Outline each blood parasite and name the species.
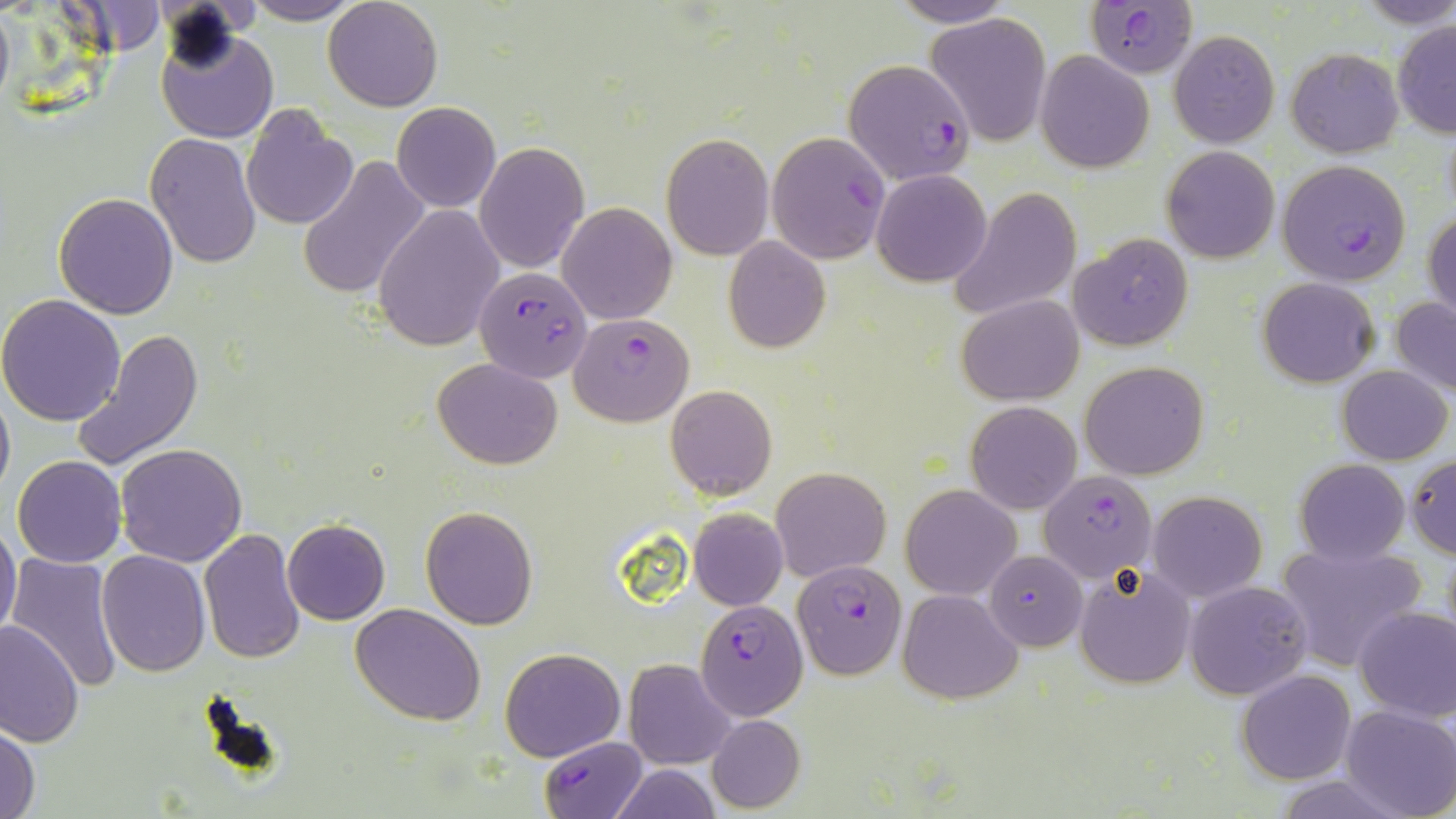

Approximate bounding boxes as named x1/y1/x2/y2 corners in pixels.
Plasmodium falciparum-infected red blood cells: (x1=1086, y1=1, x2=1198, y2=78), (x1=844, y1=60, x2=977, y2=187), (x1=1275, y1=159, x2=1412, y2=285), (x1=475, y1=264, x2=592, y2=382), (x1=569, y1=314, x2=692, y2=425), (x1=1040, y1=470, x2=1155, y2=584), (x1=984, y1=549, x2=1087, y2=650), (x1=793, y1=559, x2=905, y2=679), (x1=697, y1=600, x2=807, y2=719), (x1=538, y1=737, x2=650, y2=819).
No Plasmodium ovale, Plasmodium malariae, Plasmodium vivax, Babesia divergens, or Trypanosoma brucei observed.

Uninfected red blood cell locations: (x1=242, y1=0, x2=364, y2=24), (x1=322, y1=0, x2=444, y2=112), (x1=889, y1=0, x2=1014, y2=28), (x1=0, y1=4, x2=14, y2=115), (x1=926, y1=13, x2=1053, y2=145), (x1=1393, y1=20, x2=1456, y2=137), (x1=157, y1=26, x2=278, y2=144), (x1=1168, y1=30, x2=1279, y2=146), (x1=1285, y1=48, x2=1404, y2=158), (x1=1035, y1=50, x2=1154, y2=172), (x1=391, y1=102, x2=501, y2=212), (x1=240, y1=108, x2=358, y2=228), (x1=145, y1=132, x2=263, y2=268), (x1=765, y1=132, x2=889, y2=264), (x1=662, y1=133, x2=773, y2=260), (x1=476, y1=143, x2=588, y2=272), (x1=1162, y1=145, x2=1279, y2=263), (x1=297, y1=152, x2=430, y2=298), (x1=872, y1=169, x2=991, y2=286), (x1=947, y1=187, x2=1081, y2=320), (x1=54, y1=193, x2=179, y2=318), (x1=557, y1=202, x2=679, y2=323), (x1=373, y1=204, x2=504, y2=352), (x1=1425, y1=209, x2=1456, y2=323), (x1=1068, y1=232, x2=1193, y2=350), (x1=724, y1=236, x2=830, y2=352), (x1=1257, y1=278, x2=1380, y2=386), (x1=957, y1=294, x2=1084, y2=405), (x1=1390, y1=294, x2=1456, y2=398), (x1=0, y1=296, x2=127, y2=425), (x1=72, y1=328, x2=203, y2=470), (x1=433, y1=356, x2=562, y2=469), (x1=1081, y1=361, x2=1208, y2=479), (x1=1335, y1=365, x2=1452, y2=464), (x1=0, y1=381, x2=15, y2=505), (x1=665, y1=385, x2=776, y2=499), (x1=966, y1=401, x2=1081, y2=516), (x1=115, y1=443, x2=248, y2=567), (x1=1406, y1=453, x2=1456, y2=557), (x1=11, y1=456, x2=126, y2=568), (x1=1295, y1=458, x2=1410, y2=566), (x1=771, y1=467, x2=890, y2=582), (x1=901, y1=485, x2=1020, y2=599), (x1=1149, y1=490, x2=1267, y2=601), (x1=421, y1=507, x2=537, y2=628), (x1=689, y1=509, x2=788, y2=610), (x1=281, y1=518, x2=389, y2=625), (x1=0, y1=519, x2=22, y2=642), (x1=198, y1=528, x2=305, y2=666), (x1=1273, y1=540, x2=1427, y2=673), (x1=95, y1=551, x2=210, y2=677), (x1=7, y1=552, x2=123, y2=691), (x1=1074, y1=563, x2=1197, y2=689), (x1=1185, y1=580, x2=1312, y2=700), (x1=898, y1=589, x2=1020, y2=703), (x1=350, y1=603, x2=486, y2=726), (x1=1355, y1=606, x2=1456, y2=723), (x1=0, y1=621, x2=84, y2=749), (x1=500, y1=647, x2=625, y2=761), (x1=623, y1=659, x2=735, y2=769), (x1=1238, y1=669, x2=1356, y2=784), (x1=1338, y1=706, x2=1455, y2=819), (x1=706, y1=713, x2=806, y2=813), (x1=0, y1=724, x2=40, y2=819), (x1=608, y1=763, x2=724, y2=819), (x1=1274, y1=776, x2=1404, y2=818). Slide-level diagnosis: Plasmodium falciparum. Light microscopy. Thin blood film. Image is 1456×819 pixels. 1000x magnification. One field of a larger specimen. May-Grünwald-Giemsa stain.